Identify the preparation type.
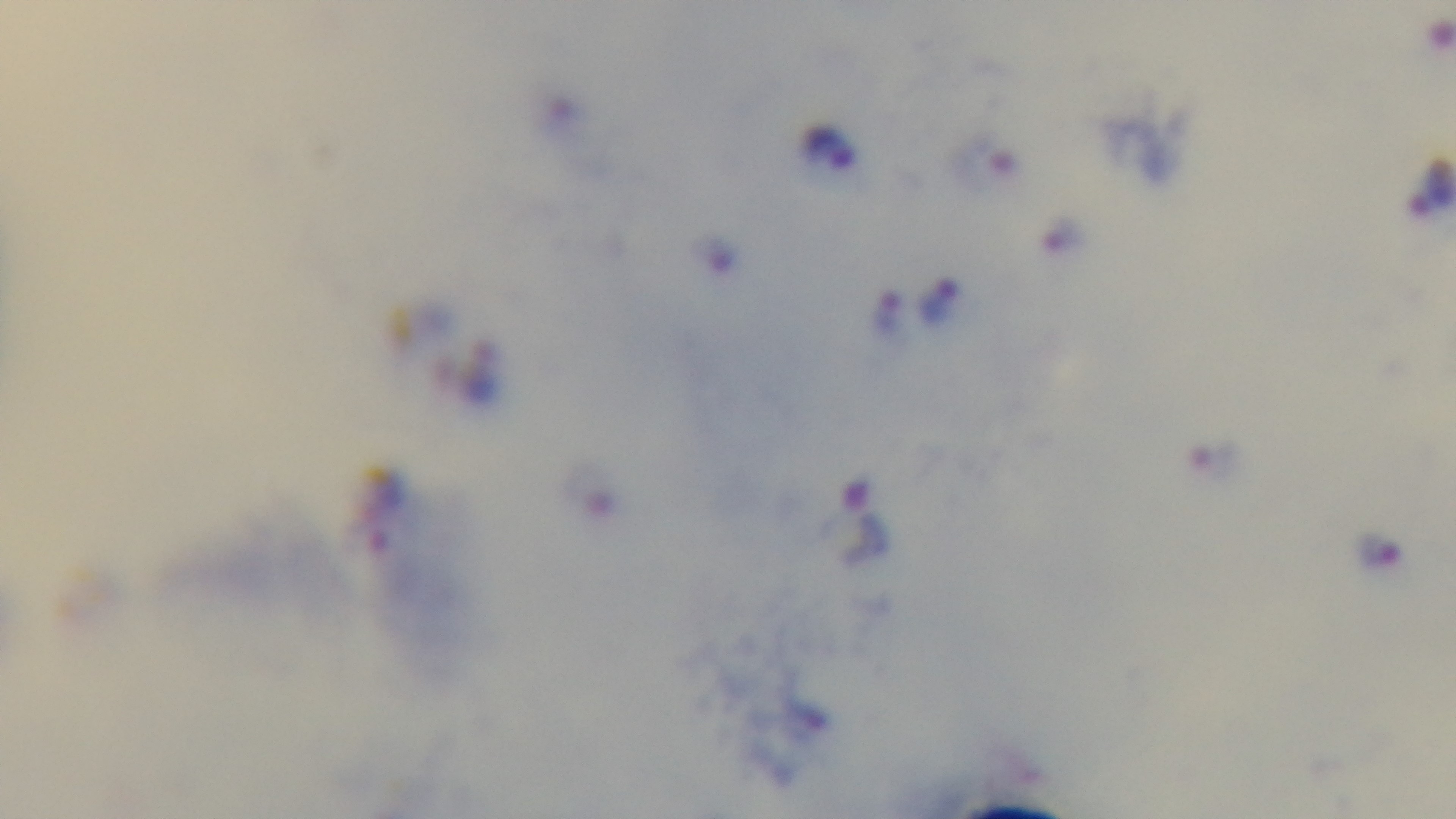
Thick.

Light microscopy. Single field of view. Giemsa stain. Malaria status: positive. Captured with a mounted 4K digital camera. 100x oil-immersion objective.